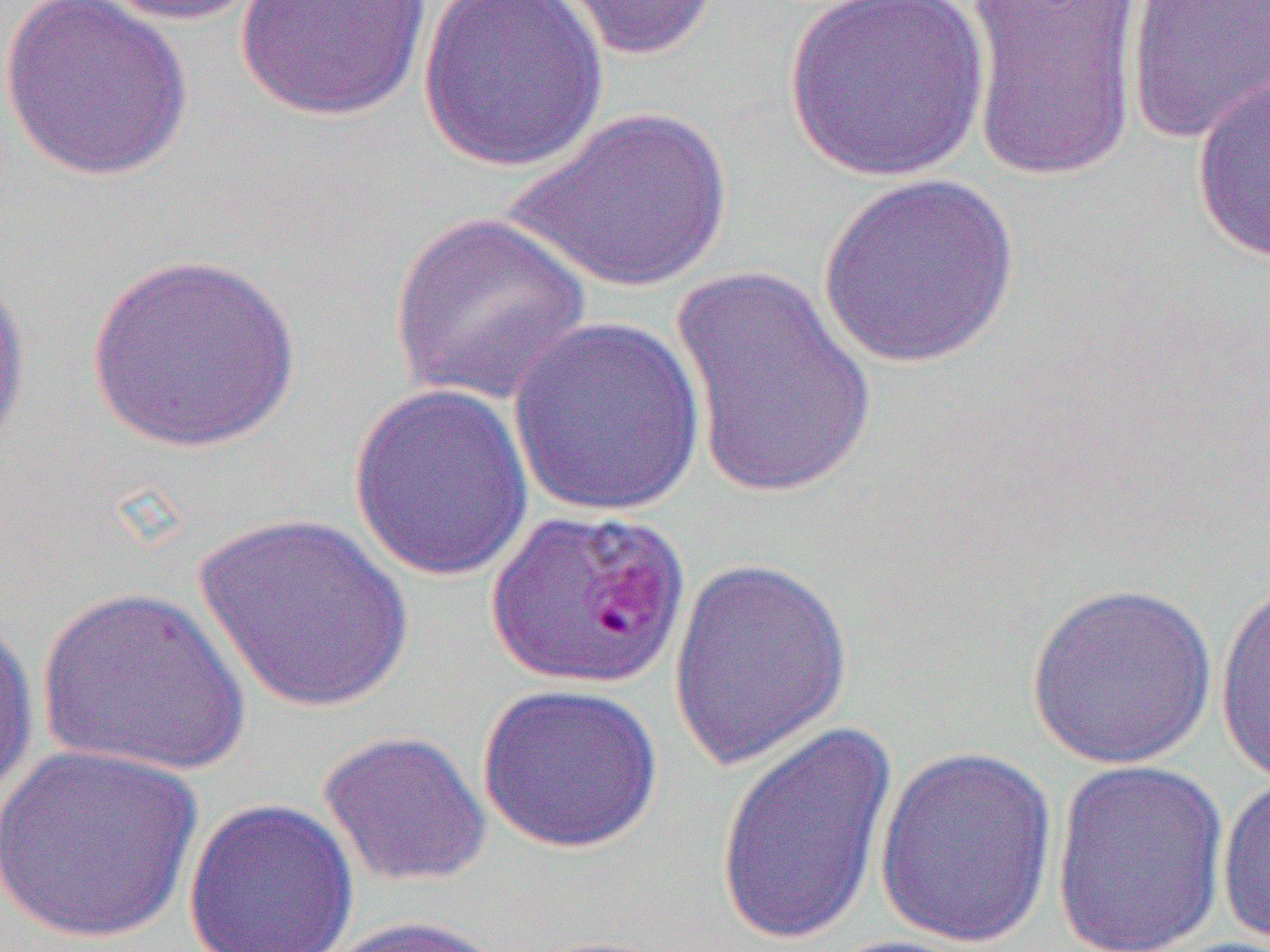
slide-level diagnosis = Plasmodium falciparum
modality = optical microscopy
preparation = thin blood smear
magnification = 1000x
uninfected red blood cell locations = approximate bounding boxes as [x1, y1, x2, y2] in pixels: [2, 0, 194, 182], [90, 0, 268, 27], [234, 0, 435, 123], [417, 0, 610, 173], [539, 0, 725, 62], [963, 0, 1144, 183], [1123, 0, 1270, 148], [784, 1, 989, 182], [1191, 75, 1270, 265], [505, 107, 732, 294], [818, 172, 1022, 370], [389, 210, 592, 407], [87, 251, 303, 455], [0, 263, 32, 472], [668, 263, 879, 501], [506, 316, 708, 519], [347, 382, 536, 583], [192, 511, 415, 714], [667, 557, 854, 772], [1215, 572, 1270, 788], [1025, 581, 1219, 770], [36, 586, 253, 779], [0, 611, 40, 815], [476, 682, 665, 854], [713, 722, 899, 948], [317, 729, 492, 889], [1, 743, 204, 944], [873, 747, 1059, 951], [1050, 759, 1230, 951], [1216, 773, 1270, 949], [183, 798, 359, 952], [320, 914, 514, 952], [815, 934, 989, 952]
field of view = single
image size = 1270×952 pixels